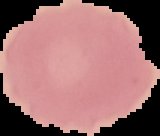
malaria status = uninfected
preparation = thin blood smear
image size = 160×136 pixels
image type = segmented cell region on a black background